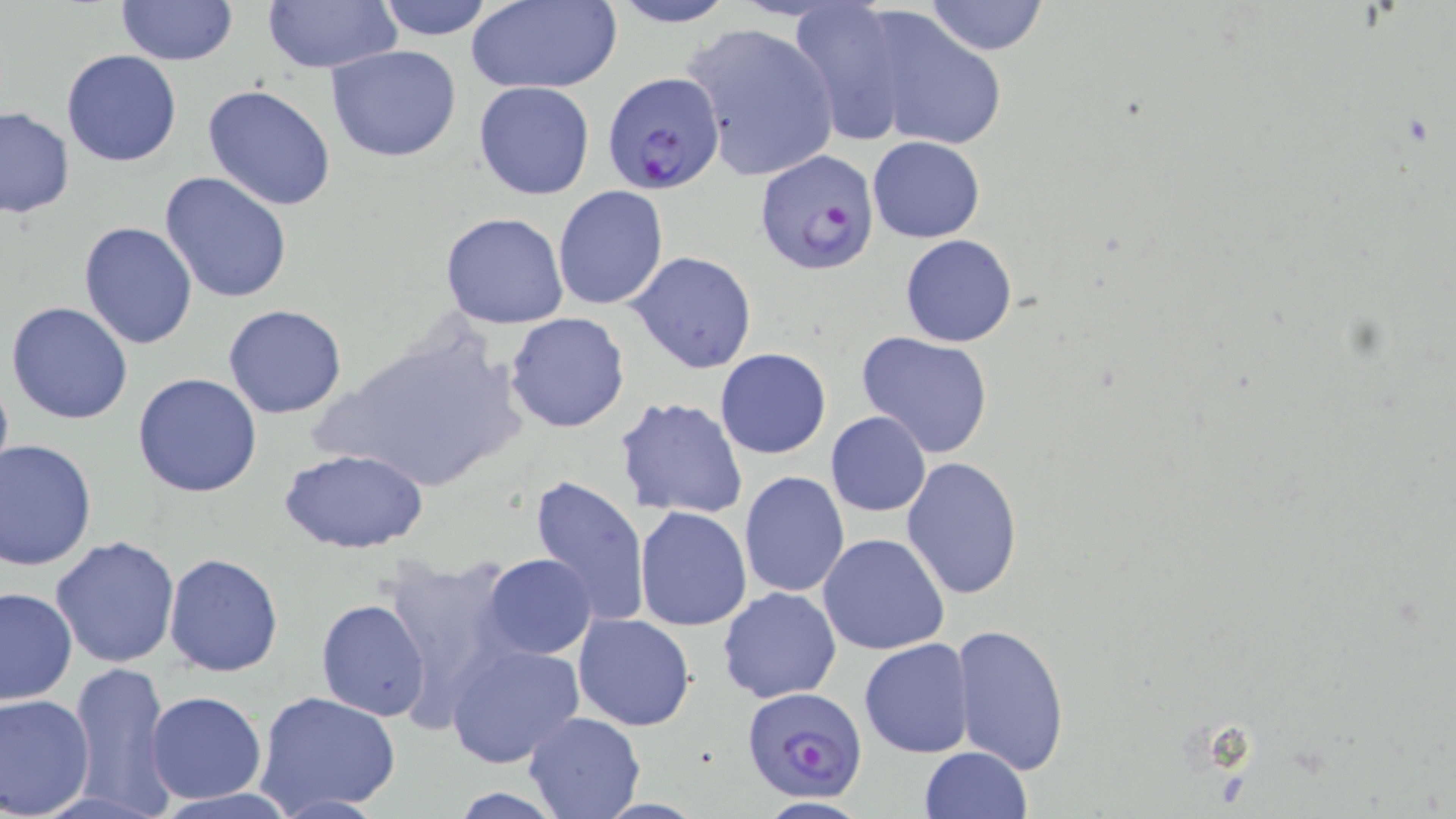

{
  "slide_level_diagnosis": "Plasmodium falciparum",
  "uninfected_red_blood_cell_locations": "approximate bounding boxes as named x1/y1/x2/y2 corners in pixels: (x1=116, y1=0, x2=237, y2=65), (x1=261, y1=0, x2=401, y2=72), (x1=373, y1=0, x2=495, y2=41), (x1=605, y1=0, x2=737, y2=28), (x1=465, y1=1, x2=620, y2=93), (x1=924, y1=1, x2=1048, y2=55), (x1=787, y1=3, x2=920, y2=142), (x1=858, y1=9, x2=1014, y2=153), (x1=680, y1=20, x2=843, y2=184), (x1=324, y1=45, x2=464, y2=164), (x1=62, y1=49, x2=182, y2=167), (x1=473, y1=81, x2=596, y2=200), (x1=203, y1=84, x2=337, y2=211), (x1=0, y1=106, x2=75, y2=218), (x1=867, y1=136, x2=985, y2=243), (x1=159, y1=171, x2=293, y2=305), (x1=553, y1=186, x2=670, y2=310), (x1=440, y1=211, x2=571, y2=329), (x1=78, y1=222, x2=199, y2=350), (x1=900, y1=234, x2=1017, y2=347), (x1=627, y1=251, x2=759, y2=376), (x1=5, y1=301, x2=134, y2=425), (x1=223, y1=304, x2=348, y2=418), (x1=503, y1=312, x2=630, y2=433), (x1=856, y1=331, x2=994, y2=459), (x1=715, y1=348, x2=831, y2=459), (x1=0, y1=368, x2=13, y2=491), (x1=133, y1=372, x2=261, y2=498), (x1=615, y1=396, x2=748, y2=521), (x1=825, y1=411, x2=930, y2=517), (x1=0, y1=439, x2=99, y2=571), (x1=279, y1=448, x2=429, y2=555), (x1=900, y1=456, x2=1023, y2=599), (x1=739, y1=471, x2=850, y2=597), (x1=528, y1=476, x2=648, y2=631), (x1=635, y1=505, x2=752, y2=632), (x1=817, y1=533, x2=949, y2=657), (x1=50, y1=535, x2=182, y2=669), (x1=163, y1=554, x2=282, y2=676), (x1=481, y1=554, x2=597, y2=659), (x1=378, y1=555, x2=518, y2=712), (x1=0, y1=586, x2=78, y2=706), (x1=718, y1=586, x2=842, y2=704), (x1=316, y1=598, x2=432, y2=721), (x1=572, y1=612, x2=696, y2=731), (x1=953, y1=623, x2=1070, y2=773), (x1=859, y1=638, x2=976, y2=757), (x1=445, y1=642, x2=585, y2=769), (x1=70, y1=659, x2=174, y2=817), (x1=146, y1=691, x2=266, y2=804), (x1=255, y1=691, x2=402, y2=815), (x1=0, y1=692, x2=96, y2=816), (x1=522, y1=711, x2=646, y2=819), (x1=918, y1=746, x2=1032, y2=818), (x1=751, y1=797, x2=873, y2=819)",
  "magnification": "1000x",
  "image_size": "1456×819 pixels",
  "field_of_view": "single",
  "modality": "light microscopy",
  "preparation": "thin blood film",
  "plasmodium_falciparum_infected_red_blood_cell_locations": "approximate bounding boxes as named x1/y1/x2/y2 corners in pixels: (x1=602, y1=72, x2=725, y2=195), (x1=754, y1=149, x2=878, y2=275), (x1=742, y1=687, x2=868, y2=803)",
  "stain": "May-Grünwald-Giemsa"
}